Assess the morphology of the red blood cells.
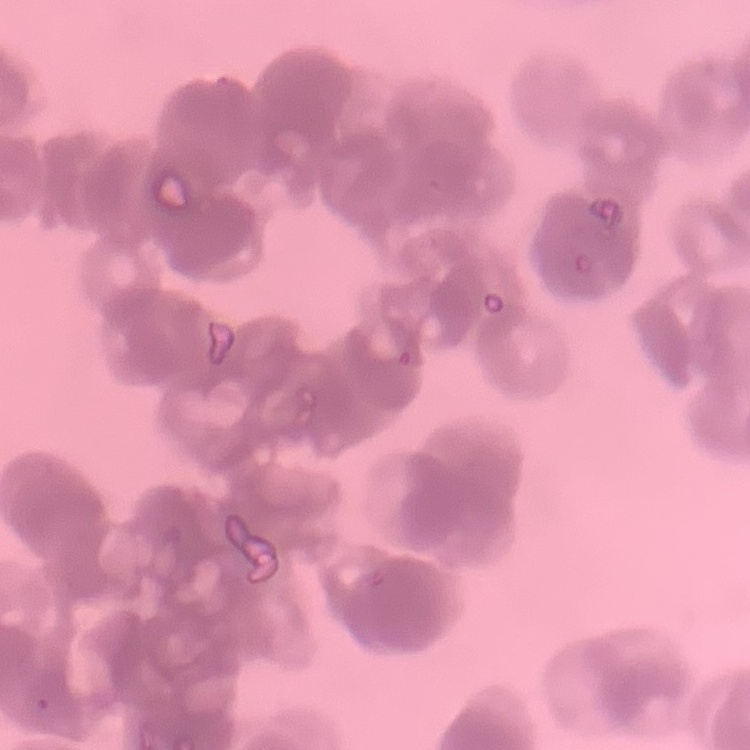
Rouleaux formation.

Summary:
  - Preparation: thin blood smear
  - Image type: square crop of a larger photomicrograph
  - Stain: Field's or Giemsa